Classify this cell by malaria status.
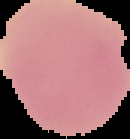

It is uninfected.

Image is 130×139 pixels. The area outside the segmented cell region is set to black. From a thin blood smear.